Comment on the morphology of the erythrocytes.
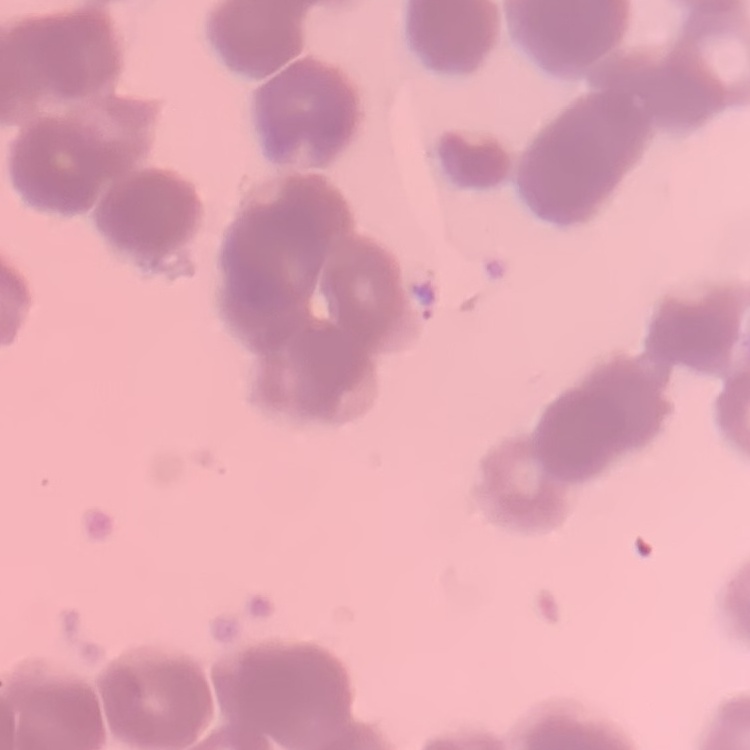
Rouleaux formation.

Summary:
  - Preparation: thin peripheral smear
  - Stain: Field's or Giemsa
  - Image type: square crop of a larger photomicrograph